Mark where leukocytes are.
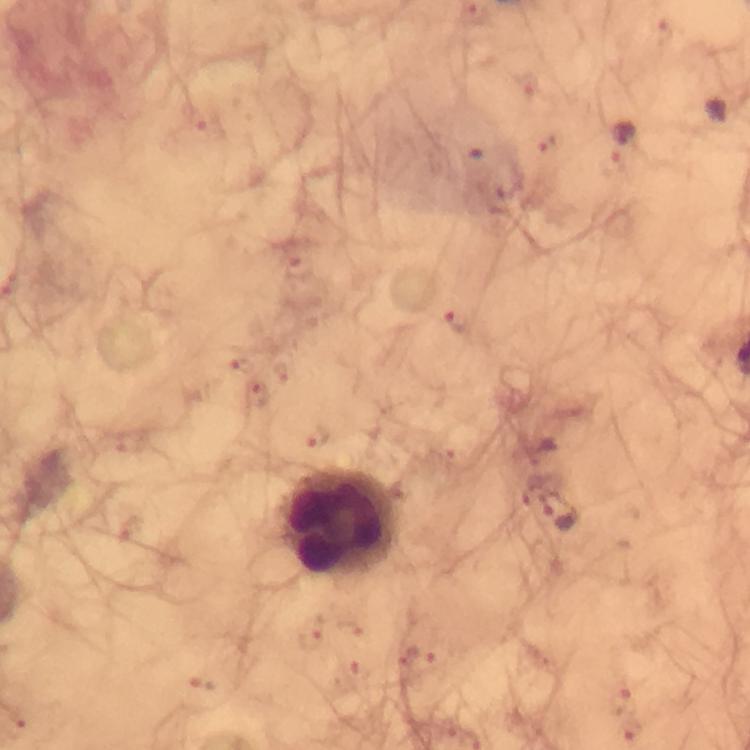

Approximate centers as {x, y} in pixels.
Leukocytes: {342, 524}.

Summary:
  - Malaria parasite locations: {457, 321}, {561, 507}
  - Preparation: thick blood smear
  - Image size: 750×750 pixels
  - Immersion oil: used
  - Capture: smartphone mounted on the microscope
  - Stain: Giemsa
  - Cropped from: a single field of view
  - Magnification: 100x
  - Context: from a diagnostic examination for malaria